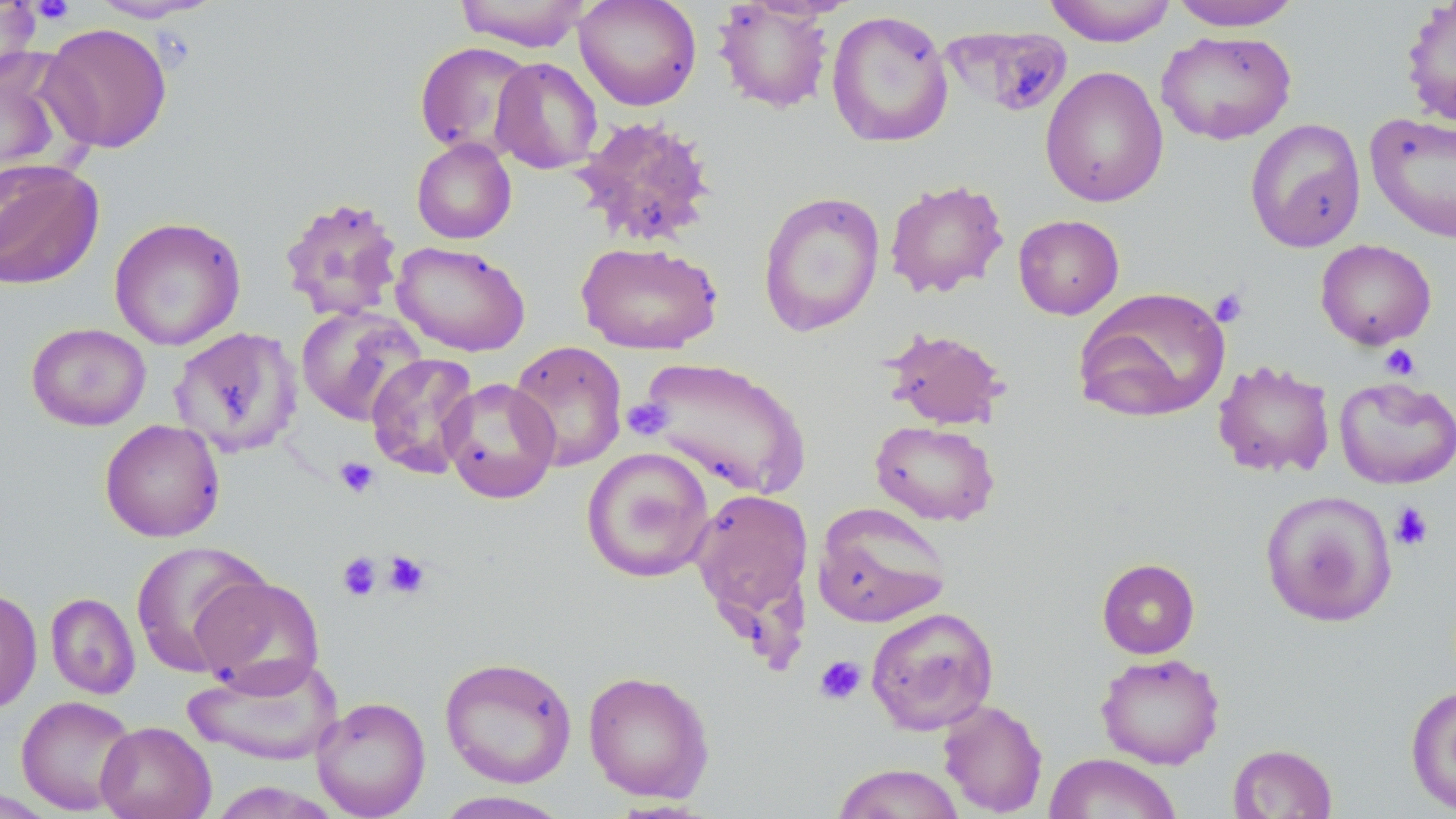
slide_level_diagnosis: negative for blood parasites
uninfected_red_blood_cell_locations: 'approximate bounding boxes as (x1, y1, x2, y2) in pixels: (0, 0, 42, 84), (87, 0, 222, 23), (455, 0, 591, 52), (574, 0, 702, 111), (1043, 0, 1177, 46), (1167, 0, 1304, 31), (1400, 0, 1456, 128), (713, 1, 834, 113), (826, 9, 954, 147), (39, 23, 174, 153), (946, 26, 1071, 117), (1156, 30, 1296, 146), (414, 41, 536, 159), (0, 46, 85, 186), (490, 57, 603, 174), (1040, 66, 1169, 208), (1365, 111, 1456, 243), (570, 114, 718, 249), (1245, 118, 1366, 253), (411, 138, 517, 244), (0, 157, 104, 291), (884, 179, 1009, 298), (757, 191, 886, 337), (278, 195, 405, 322), (1013, 214, 1124, 320), (108, 217, 246, 351), (1315, 239, 1437, 350), (392, 240, 531, 357), (576, 241, 723, 355), (1074, 287, 1231, 424), (296, 305, 427, 426), (26, 323, 152, 432), (169, 326, 303, 459), (882, 327, 1010, 430), (508, 340, 628, 473), (366, 352, 480, 479), (635, 356, 811, 499), (1212, 359, 1336, 478), (1333, 376, 1456, 490), (440, 377, 560, 504), (99, 419, 226, 543), (870, 420, 1000, 526), (581, 446, 715, 583), (689, 489, 814, 627), (1259, 490, 1397, 627), (812, 503, 951, 628), (130, 541, 270, 678), (1097, 558, 1200, 658), (191, 573, 325, 695), (0, 587, 42, 713), (45, 592, 140, 699), (865, 606, 1000, 734), (1095, 653, 1225, 769), (183, 656, 343, 766), (439, 656, 577, 788), (583, 670, 714, 803), (1405, 684, 1456, 815), (16, 695, 138, 815), (311, 696, 431, 818), (937, 699, 1048, 817), (95, 720, 216, 819), (1228, 743, 1338, 818), (1043, 752, 1182, 819), (830, 763, 966, 819), (431, 790, 574, 818)'
image_size: 1456×819 pixels
modality: optical microscopy
stain: May-Grünwald-Giemsa
field_of_view: one of a larger specimen
platelet_locations: 'approximate bounding boxes as (x1, y1, x2, y2) in pixels: (29, 0, 75, 25), (1210, 288, 1248, 327), (1380, 344, 1420, 380), (623, 398, 671, 441), (335, 457, 379, 499), (1390, 502, 1434, 551), (382, 550, 432, 599), (337, 551, 383, 601), (814, 655, 866, 704)'
preparation: thin blood smear
magnification: 1000x